State which parasite is depicted.
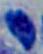

Toxoplasma gondii.

Micrograph. 1000x magnification.